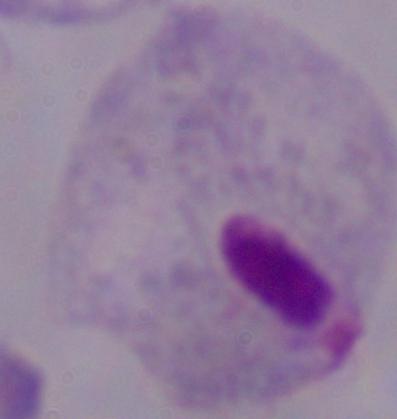

Captured at 1000x magnification. A trichomonad is seen. Photomicrograph.